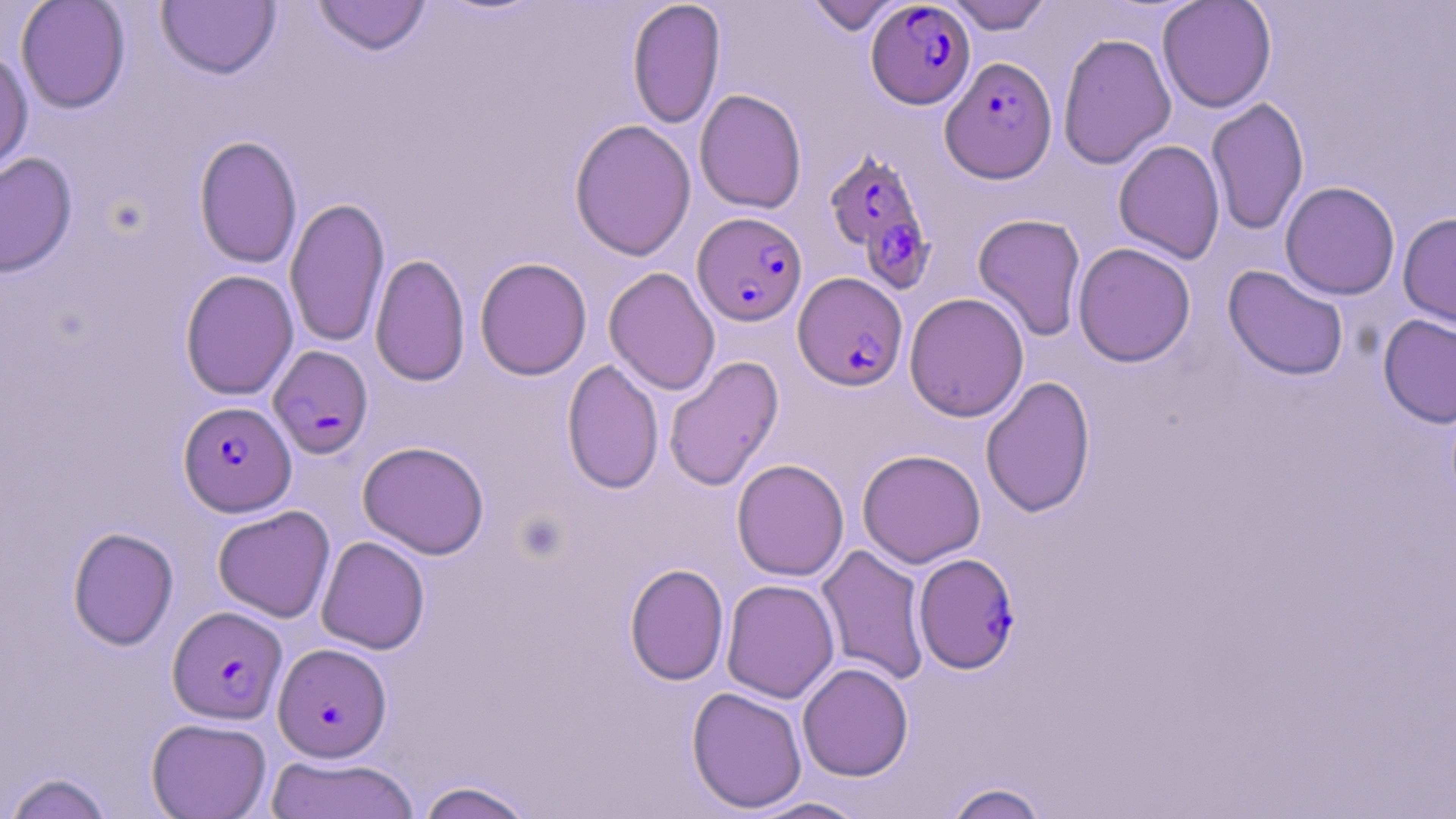

Approximate bounding boxes as named x1/y1/x2/y2 corners in pixels. Plasmodium falciparum-infected red blood cell locations: (x1=866, y1=2, x2=976, y2=109), (x1=939, y1=57, x2=1056, y2=182), (x1=825, y1=148, x2=934, y2=288), (x1=692, y1=214, x2=808, y2=328), (x1=794, y1=272, x2=908, y2=391), (x1=269, y1=345, x2=373, y2=458), (x1=178, y1=401, x2=296, y2=516), (x1=913, y1=553, x2=1019, y2=673), (x1=168, y1=605, x2=287, y2=724), (x1=273, y1=642, x2=392, y2=762). Uninfected red blood cell locations: (x1=15, y1=0, x2=130, y2=114), (x1=311, y1=0, x2=432, y2=56), (x1=626, y1=0, x2=726, y2=130), (x1=805, y1=0, x2=905, y2=35), (x1=944, y1=0, x2=1053, y2=34), (x1=1157, y1=0, x2=1276, y2=113), (x1=156, y1=1, x2=280, y2=80), (x1=1057, y1=32, x2=1176, y2=170), (x1=0, y1=48, x2=34, y2=179), (x1=694, y1=89, x2=807, y2=214), (x1=1206, y1=97, x2=1309, y2=236), (x1=569, y1=119, x2=696, y2=261), (x1=193, y1=135, x2=302, y2=269), (x1=1114, y1=139, x2=1225, y2=264), (x1=0, y1=152, x2=78, y2=277), (x1=1280, y1=181, x2=1400, y2=300), (x1=285, y1=197, x2=390, y2=348), (x1=1398, y1=212, x2=1456, y2=331), (x1=972, y1=213, x2=1087, y2=341), (x1=1072, y1=242, x2=1196, y2=367), (x1=370, y1=253, x2=470, y2=387), (x1=474, y1=257, x2=592, y2=381), (x1=1222, y1=265, x2=1349, y2=381), (x1=604, y1=267, x2=721, y2=395), (x1=180, y1=269, x2=299, y2=401), (x1=904, y1=292, x2=1029, y2=422), (x1=1378, y1=314, x2=1456, y2=429), (x1=663, y1=355, x2=783, y2=492), (x1=561, y1=359, x2=664, y2=495), (x1=980, y1=376, x2=1095, y2=518), (x1=358, y1=441, x2=489, y2=559), (x1=857, y1=449, x2=986, y2=568), (x1=731, y1=458, x2=849, y2=581), (x1=212, y1=505, x2=336, y2=622), (x1=67, y1=526, x2=179, y2=650), (x1=316, y1=536, x2=430, y2=654), (x1=816, y1=544, x2=931, y2=686), (x1=624, y1=562, x2=729, y2=685), (x1=721, y1=578, x2=839, y2=703), (x1=797, y1=662, x2=913, y2=781), (x1=687, y1=687, x2=807, y2=814), (x1=146, y1=717, x2=272, y2=818), (x1=265, y1=754, x2=419, y2=819), (x1=2, y1=771, x2=116, y2=819), (x1=415, y1=780, x2=537, y2=819), (x1=943, y1=781, x2=1050, y2=819), (x1=744, y1=795, x2=873, y2=818). Slide-level diagnosis: Plasmodium falciparum. Optical microscopy. 1000x magnification. May-Grünwald-Giemsa-stained preparation. Image is 1456×819 pixels. Thin blood film. One field of a larger specimen.